Report the malaria status of this cell.
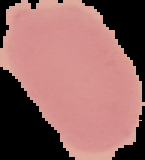

It is uninfected.

From a thin blood smear. Image is 145×160 pixels. Cell region segmented out of the field of view; the surrounding area is masked to black.